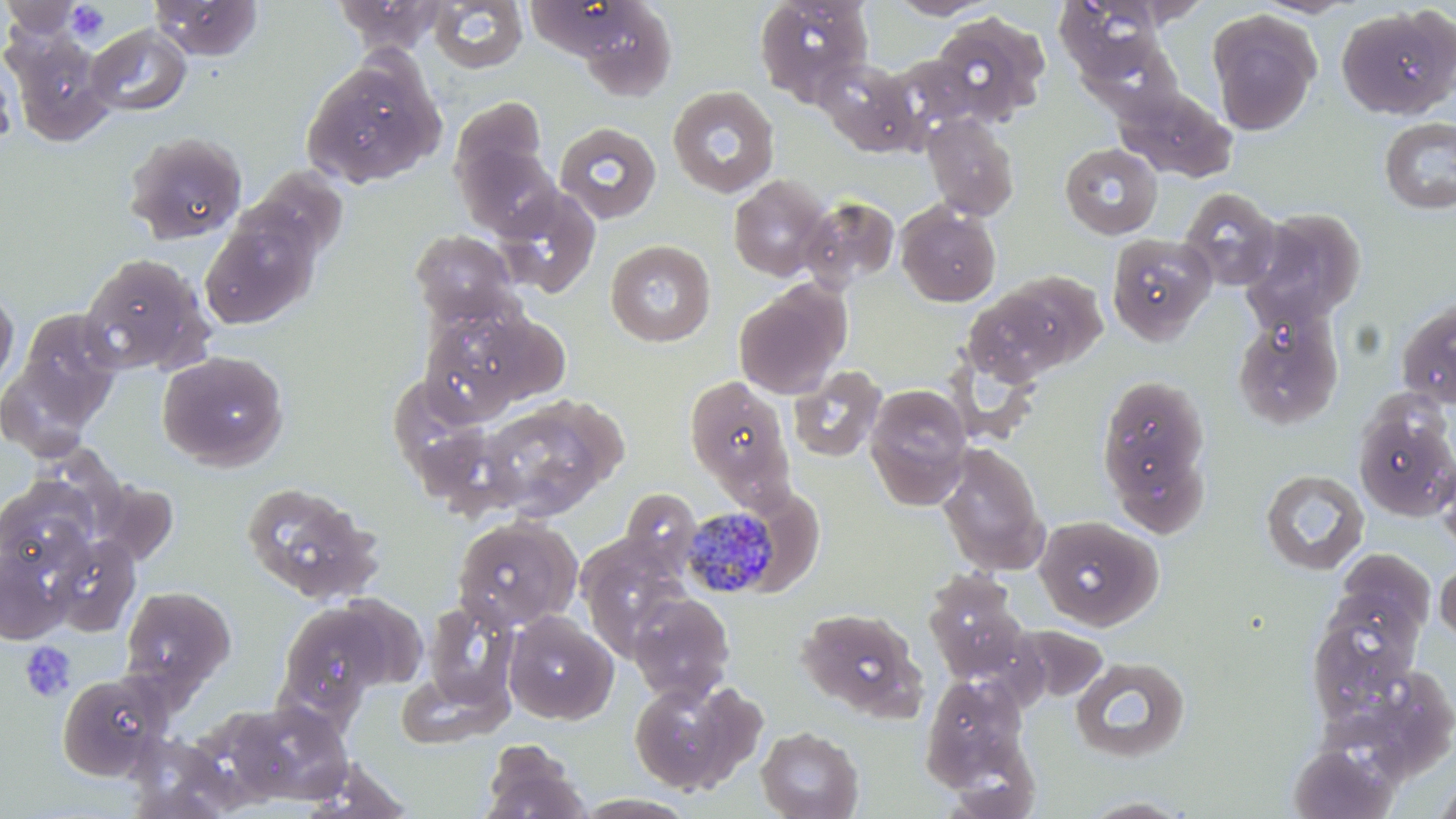

Summary:
  - Coordinate format: approximate bounding boxes as [x1, y1, x2, y2] in pixels
  - Plasmodium malariae-infected red blood cell locations: [681, 509, 782, 599]
  - Platelet locations: [66, 2, 109, 45], [20, 641, 76, 703]
  - Uninfected red blood cell locations: [1, 0, 86, 42], [150, 0, 263, 60], [334, 0, 445, 55], [754, 0, 874, 104], [886, 0, 998, 19], [1056, 0, 1168, 79], [1114, 0, 1213, 28], [428, 1, 527, 74], [575, 2, 677, 101], [1336, 6, 1456, 120], [930, 12, 1051, 124], [1207, 12, 1320, 135], [86, 24, 192, 116], [5, 30, 115, 144], [1084, 33, 1182, 117], [884, 54, 989, 144], [0, 56, 18, 149], [301, 56, 444, 188], [815, 58, 920, 155], [1116, 85, 1237, 183], [667, 86, 779, 198], [450, 97, 549, 193], [922, 113, 1020, 221], [1379, 116, 1456, 215], [553, 122, 662, 225], [124, 131, 247, 245], [455, 138, 562, 238], [1059, 143, 1162, 239], [246, 168, 350, 264], [728, 175, 831, 282], [492, 186, 601, 297], [1179, 187, 1283, 290], [798, 196, 900, 291], [896, 202, 1001, 307], [1245, 206, 1369, 326], [200, 212, 321, 329], [411, 230, 518, 326], [1106, 233, 1217, 345], [605, 239, 716, 347], [77, 254, 216, 376], [734, 281, 850, 399], [0, 285, 19, 396], [959, 285, 1079, 385], [1396, 297, 1456, 409], [418, 307, 537, 423], [1231, 307, 1345, 431], [13, 309, 123, 421], [156, 350, 289, 471], [944, 352, 1043, 446], [788, 365, 886, 463], [1097, 373, 1211, 514], [683, 374, 795, 501], [863, 384, 973, 509], [478, 400, 614, 521], [1354, 406, 1456, 521], [937, 442, 1050, 576], [1436, 456, 1456, 557], [1259, 469, 1370, 576], [240, 481, 383, 605], [620, 488, 701, 572], [451, 515, 583, 632], [1033, 515, 1162, 630], [47, 534, 142, 636], [0, 544, 74, 644], [1435, 558, 1456, 645], [923, 571, 1031, 685], [119, 586, 236, 695], [628, 592, 735, 704], [1307, 598, 1424, 712], [276, 600, 396, 718], [422, 602, 517, 711], [797, 607, 928, 721], [503, 611, 618, 725], [1070, 656, 1191, 764], [394, 666, 513, 748], [56, 672, 172, 780], [921, 675, 1032, 787], [628, 677, 766, 796], [217, 700, 353, 806], [756, 727, 864, 819], [123, 732, 243, 818], [481, 740, 590, 819], [1287, 744, 1397, 818], [1433, 773, 1456, 819], [1077, 795, 1197, 818]
  - Slide-level diagnosis: Plasmodium malariae
  - Preparation: thin blood film
  - Modality: light microscopy
  - Field of view: single
  - Magnification: 1000x
  - Image size: 1456×819 pixels
  - Stain: May-Grünwald-Giemsa